Assess the morphology of the erythrocytes.
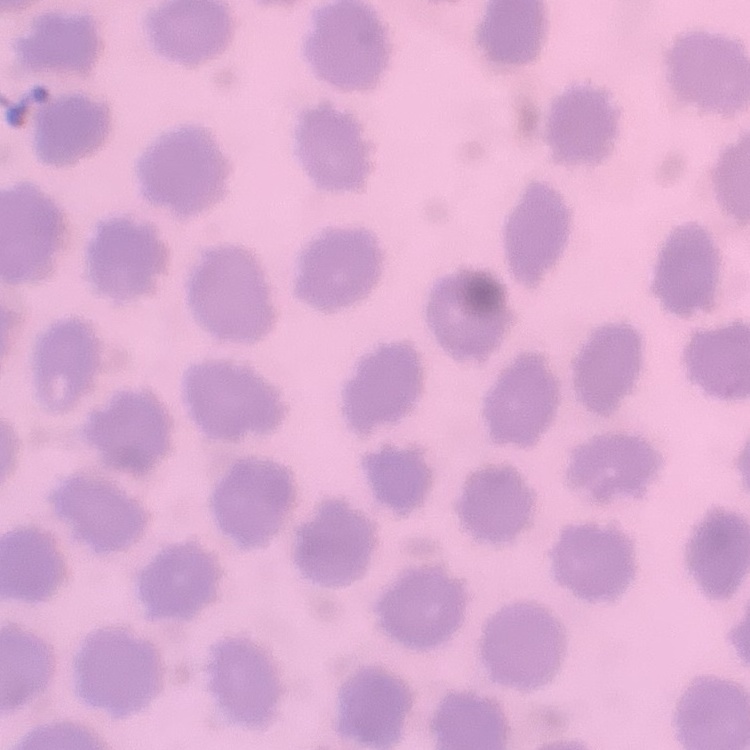

They show no rouleaux formation.

One tile cut from a larger photomicrograph. Thin blood smear. Stained with either Field's or Giemsa.